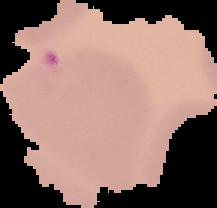 Malaria status: parasitized. Image is 217×208 pixels. From a thin blood film. Cell region segmented out of the field of view; the surrounding area is masked to black.